Report the malaria status of this cell.
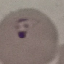
Parasitized.

Summary:
  - Preparation: thin smear
  - Stain: Giemsa
  - Image type: cell patch, automatically extracted from a larger field of view and resized to 64 × 64 pixels
  - Capture: smartphone camera at the microscope eyepiece